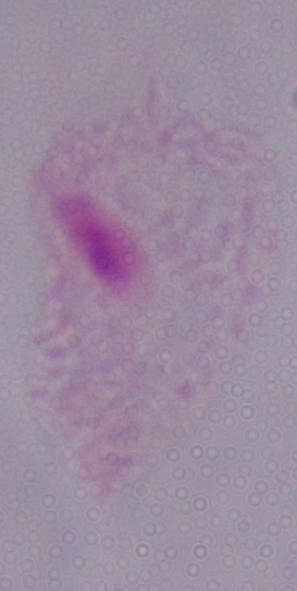
magnification = 1000x
modality = photomicrograph
identification = trichomonad